Identify the parasite.
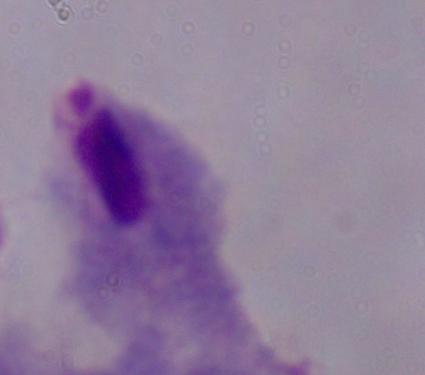

A trichomonad.

magnification = 1000x
modality = micrograph